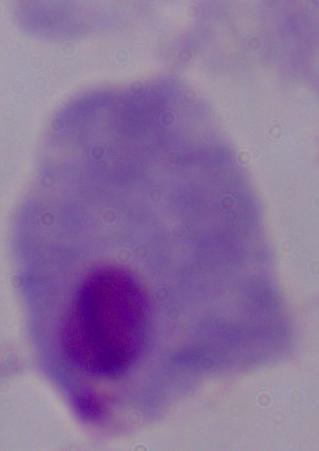
magnification = 1000x
modality = photomicrograph
identification = trichomonad